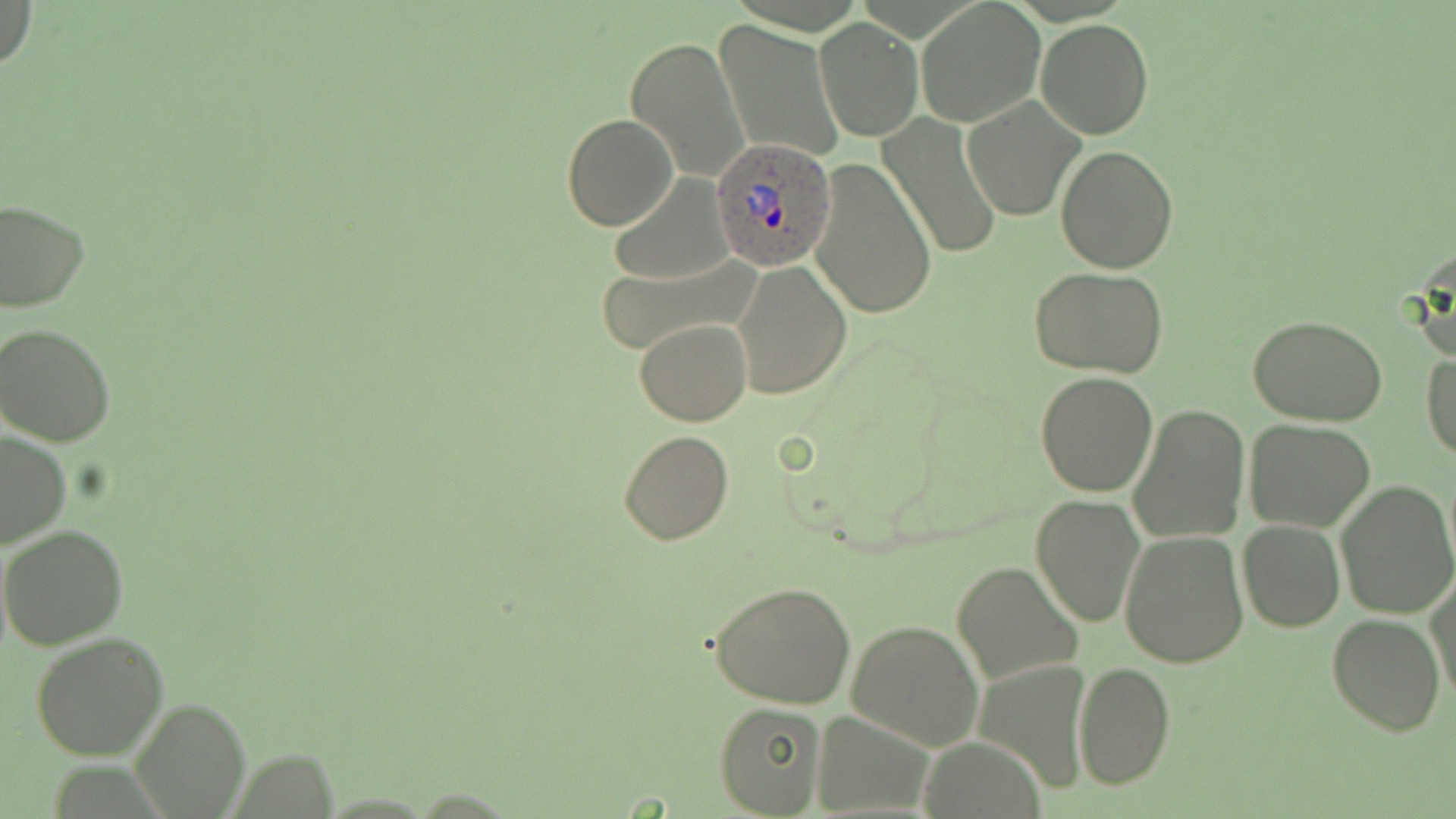
Approximate bounding boxes as [x1, y1, x2, y2] in pixels. Plasmodium ovale-infected red blood cell locations: [712, 141, 836, 271]. Uninfected red blood cell locations: [1, 0, 37, 74], [917, 2, 1044, 126], [815, 18, 922, 141], [1035, 19, 1154, 139], [714, 20, 844, 163], [625, 35, 751, 182], [962, 97, 1083, 221], [879, 113, 1003, 261], [562, 114, 677, 231], [1055, 145, 1178, 273], [806, 157, 937, 319], [608, 174, 736, 285], [0, 198, 89, 313], [1408, 244, 1456, 368], [594, 258, 757, 358], [732, 258, 853, 402], [1029, 267, 1173, 380], [1248, 313, 1391, 424], [635, 318, 752, 426], [0, 321, 120, 447], [1422, 350, 1456, 461], [1035, 371, 1159, 496], [1129, 404, 1249, 544], [1243, 419, 1374, 532], [0, 429, 71, 550], [618, 429, 736, 546], [1336, 479, 1456, 619], [1030, 494, 1145, 627], [1238, 520, 1345, 632], [0, 524, 129, 650], [1120, 529, 1250, 668], [951, 559, 1079, 686], [1428, 571, 1455, 703], [709, 579, 856, 709], [1327, 613, 1445, 735], [846, 619, 984, 752], [29, 632, 170, 762], [1073, 660, 1175, 790], [132, 697, 248, 818], [715, 703, 827, 816], [814, 708, 933, 816], [922, 740, 1048, 817]. Slide-level diagnosis: Plasmodium ovale. Optical microscopy. Thin blood film. Single field of view. Captured at 1000x magnification. Image is 1456×819 pixels. May-Grünwald-Giemsa-stained preparation.